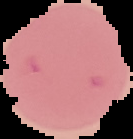
result = no Plasmodium parasites detected
image size = 133×139 pixels
preparation = thin blood smear
image type = segmented cell region with the area outside set to black